State which parasite is depicted.
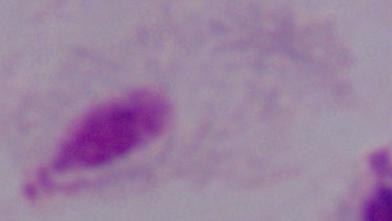
This is a trichomonad.

1000x magnification. Micrograph.